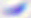

Summary:
  - Modality: photomicrograph
  - Magnification: 400x
  - Identification: Toxoplasma gondii